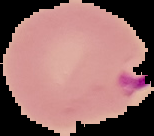
From a thin blood film. Image is 154×136 pixels. Cell region segmented out of the field of view; the surrounding area is masked to black. Malaria status: parasitized.